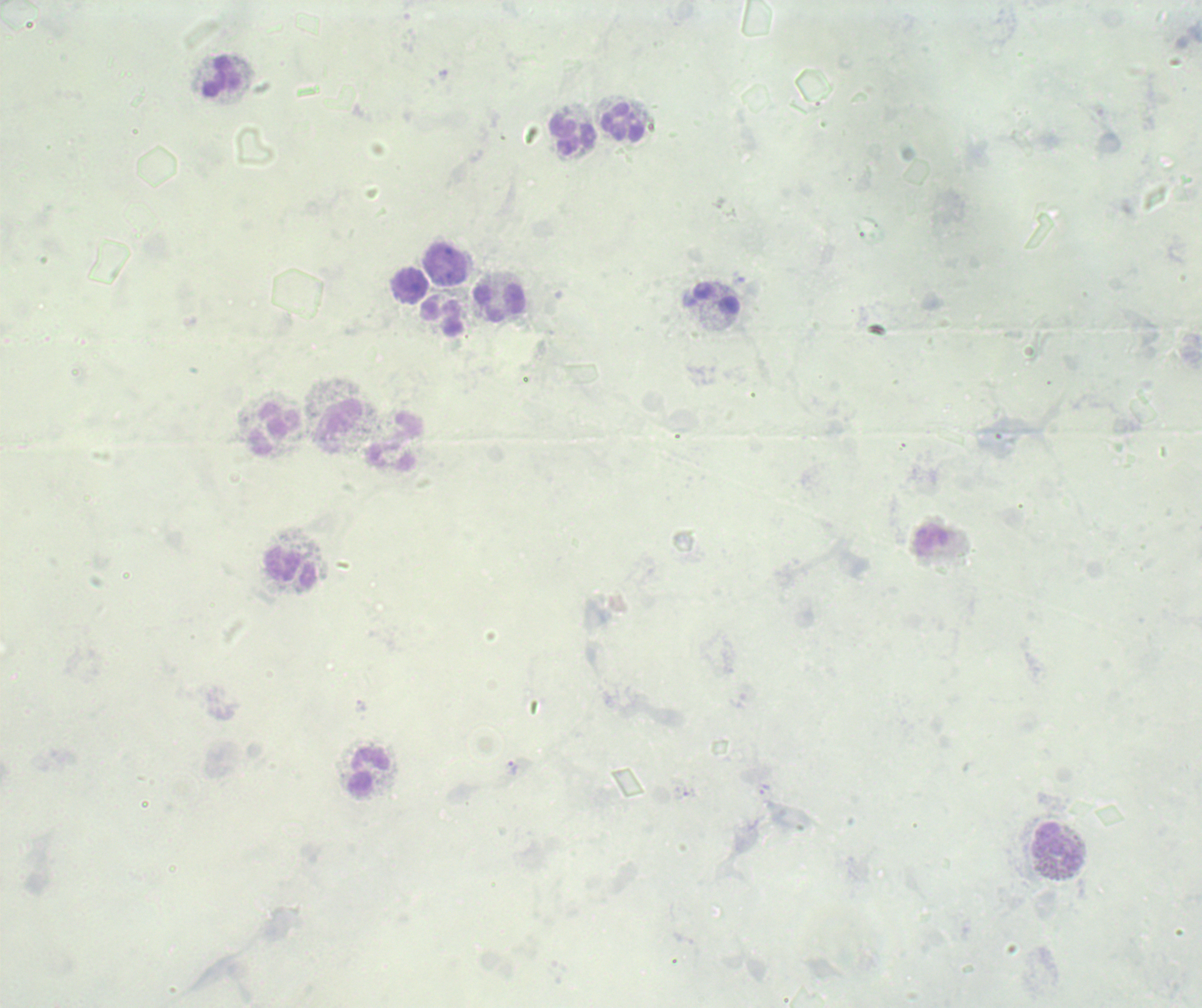

coordinate format = approximate object centers, in pixels from the top-left corner
trophozoite locations = (x=513, y=768)
leukocyte locations = (x=224, y=78), (x=623, y=123), (x=573, y=135), (x=445, y=265), (x=409, y=284), (x=716, y=298), (x=499, y=303), (x=443, y=317), (x=339, y=422), (x=275, y=429), (x=392, y=440), (x=290, y=566), (x=369, y=772), (x=1059, y=847)
field of view = single
stain = Romanowsky
image size = 1202×1008 pixels
preparation = thick blood smear
background quality = poor
result = positive for malaria parasites
magnification = 100x
context = previously used in a real diagnosis